Classify this cell by malaria status.
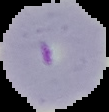
Parasitized.

Summary:
  - Image size: 109×112 pixels
  - Preparation: thin blood smear
  - Image type: cell region segmented out of the field of view; surrounding area masked to black